Identify the blood parasite species.
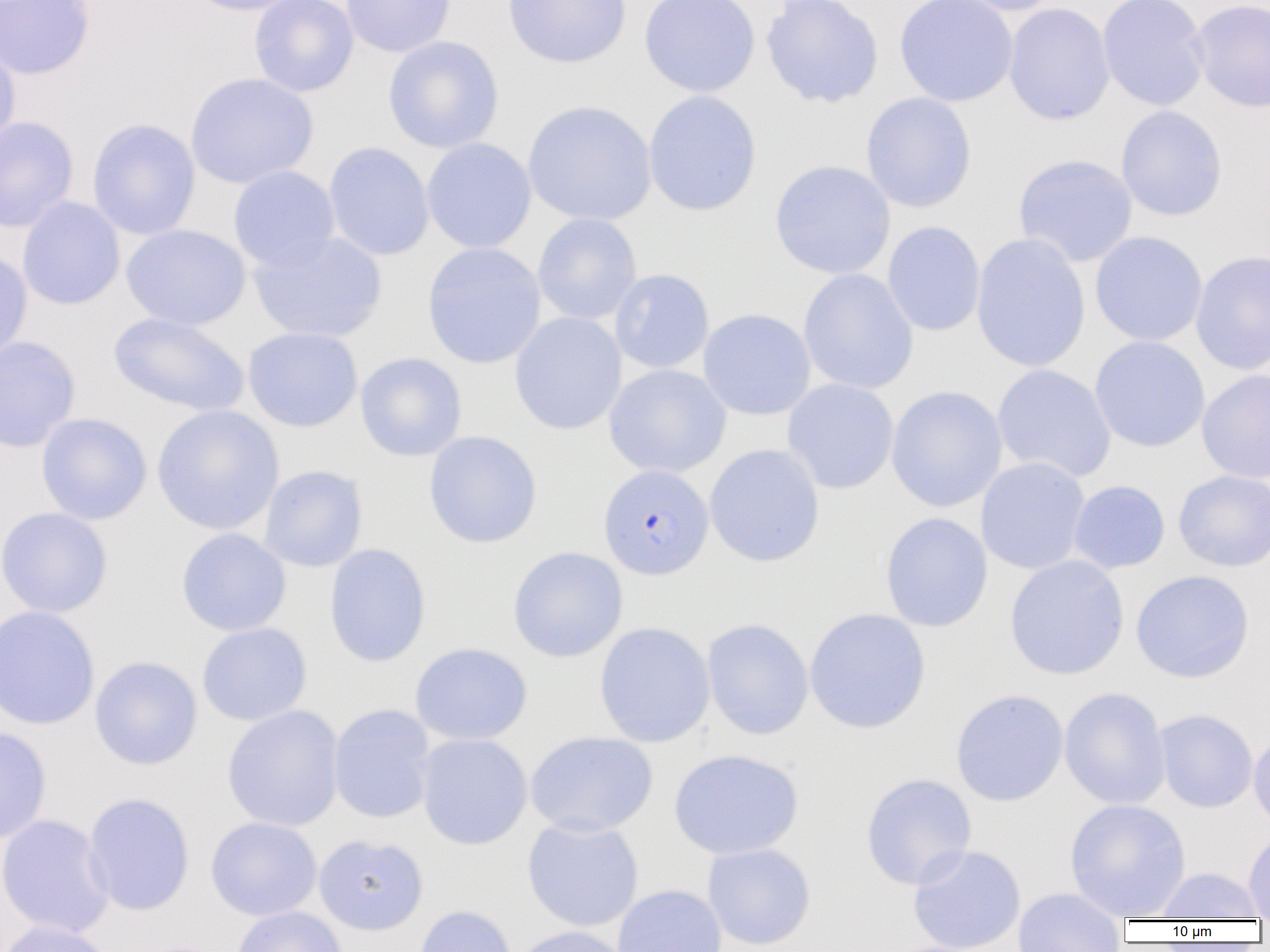
Plasmodium falciparum.

{
  "preparation": "thin blood film",
  "uninfected_red_blood_cell_locations": "approximate bounding boxes as named x1/y1/x2/y2 corners in pixels: (x1=0, y1=0, x2=96, y2=80), (x1=182, y1=0, x2=308, y2=16), (x1=249, y1=0, x2=359, y2=97), (x1=340, y1=0, x2=456, y2=58), (x1=502, y1=0, x2=632, y2=68), (x1=639, y1=0, x2=760, y2=97), (x1=760, y1=0, x2=884, y2=109), (x1=895, y1=0, x2=1018, y2=106), (x1=952, y1=0, x2=1069, y2=16), (x1=1097, y1=0, x2=1210, y2=111), (x1=1189, y1=0, x2=1270, y2=113), (x1=1003, y1=3, x2=1115, y2=125), (x1=383, y1=35, x2=504, y2=153), (x1=0, y1=40, x2=21, y2=154), (x1=185, y1=72, x2=318, y2=189), (x1=643, y1=90, x2=762, y2=216), (x1=860, y1=92, x2=977, y2=212), (x1=523, y1=100, x2=657, y2=225), (x1=1115, y1=105, x2=1228, y2=221), (x1=0, y1=116, x2=79, y2=232), (x1=87, y1=118, x2=201, y2=240), (x1=421, y1=138, x2=536, y2=253), (x1=324, y1=142, x2=434, y2=261), (x1=1013, y1=154, x2=1138, y2=267), (x1=770, y1=160, x2=895, y2=279), (x1=228, y1=165, x2=340, y2=270), (x1=17, y1=197, x2=125, y2=310), (x1=532, y1=213, x2=642, y2=325), (x1=882, y1=221, x2=986, y2=336), (x1=121, y1=224, x2=250, y2=330), (x1=248, y1=230, x2=387, y2=343), (x1=1089, y1=231, x2=1208, y2=347), (x1=971, y1=233, x2=1090, y2=373), (x1=422, y1=242, x2=546, y2=368), (x1=0, y1=248, x2=33, y2=363), (x1=1190, y1=250, x2=1270, y2=375), (x1=798, y1=268, x2=919, y2=395), (x1=610, y1=269, x2=714, y2=374), (x1=698, y1=308, x2=816, y2=420), (x1=510, y1=312, x2=627, y2=435), (x1=109, y1=313, x2=250, y2=417), (x1=243, y1=327, x2=363, y2=432), (x1=0, y1=336, x2=81, y2=452), (x1=1089, y1=336, x2=1210, y2=452), (x1=355, y1=352, x2=467, y2=461), (x1=604, y1=363, x2=731, y2=478), (x1=992, y1=364, x2=1116, y2=483), (x1=1196, y1=369, x2=1270, y2=484), (x1=782, y1=378, x2=899, y2=494), (x1=886, y1=385, x2=1007, y2=513), (x1=152, y1=405, x2=284, y2=535), (x1=36, y1=413, x2=152, y2=525), (x1=423, y1=431, x2=542, y2=548), (x1=704, y1=443, x2=825, y2=567), (x1=975, y1=457, x2=1091, y2=575), (x1=258, y1=465, x2=368, y2=572), (x1=1173, y1=470, x2=1270, y2=572), (x1=1068, y1=480, x2=1170, y2=574), (x1=0, y1=507, x2=113, y2=618), (x1=880, y1=512, x2=993, y2=632), (x1=176, y1=528, x2=291, y2=636), (x1=324, y1=543, x2=431, y2=667), (x1=508, y1=546, x2=628, y2=662), (x1=1005, y1=555, x2=1129, y2=680), (x1=1131, y1=570, x2=1254, y2=683), (x1=0, y1=605, x2=100, y2=730), (x1=804, y1=608, x2=931, y2=734), (x1=701, y1=619, x2=814, y2=740), (x1=594, y1=621, x2=716, y2=747), (x1=197, y1=622, x2=312, y2=726), (x1=410, y1=642, x2=532, y2=745), (x1=89, y1=656, x2=203, y2=770), (x1=1059, y1=686, x2=1171, y2=810), (x1=950, y1=689, x2=1069, y2=806), (x1=222, y1=705, x2=344, y2=832), (x1=328, y1=705, x2=437, y2=824), (x1=1154, y1=709, x2=1258, y2=813), (x1=0, y1=725, x2=52, y2=844), (x1=1248, y1=730, x2=1270, y2=833), (x1=525, y1=731, x2=658, y2=837), (x1=416, y1=733, x2=533, y2=849), (x1=669, y1=749, x2=804, y2=859), (x1=861, y1=773, x2=977, y2=890), (x1=82, y1=792, x2=195, y2=916), (x1=1064, y1=798, x2=1191, y2=920), (x1=0, y1=813, x2=115, y2=938), (x1=206, y1=817, x2=322, y2=920), (x1=521, y1=817, x2=644, y2=932), (x1=1243, y1=828, x2=1270, y2=919), (x1=314, y1=833, x2=428, y2=935), (x1=702, y1=843, x2=816, y2=950), (x1=907, y1=843, x2=1026, y2=952), (x1=1153, y1=867, x2=1267, y2=921), (x1=612, y1=884, x2=727, y2=952), (x1=1012, y1=887, x2=1128, y2=951), (x1=413, y1=905, x2=517, y2=952), (x1=231, y1=906, x2=347, y2=952), (x1=0, y1=920, x2=119, y2=952), (x1=510, y1=925, x2=632, y2=952)",
  "image_size": "1270×952 pixels",
  "plasmodium_falciparum_infected_red_blood_cell_locations": "approximate bounding boxes as named x1/y1/x2/y2 corners in pixels: (x1=598, y1=463, x2=714, y2=580)",
  "field_of_view": "single",
  "modality": "optical microscopy",
  "magnification": "1000x"
}